Classify this cell by malaria status.
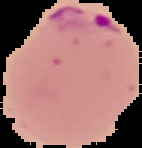
Parasitized.

Summary:
  - Preparation: thin blood film
  - Image size: 142×148 pixels
  - Image type: cell region segmented out of the field of view; surrounding area masked to black